Describe the morphology of the red blood cells.
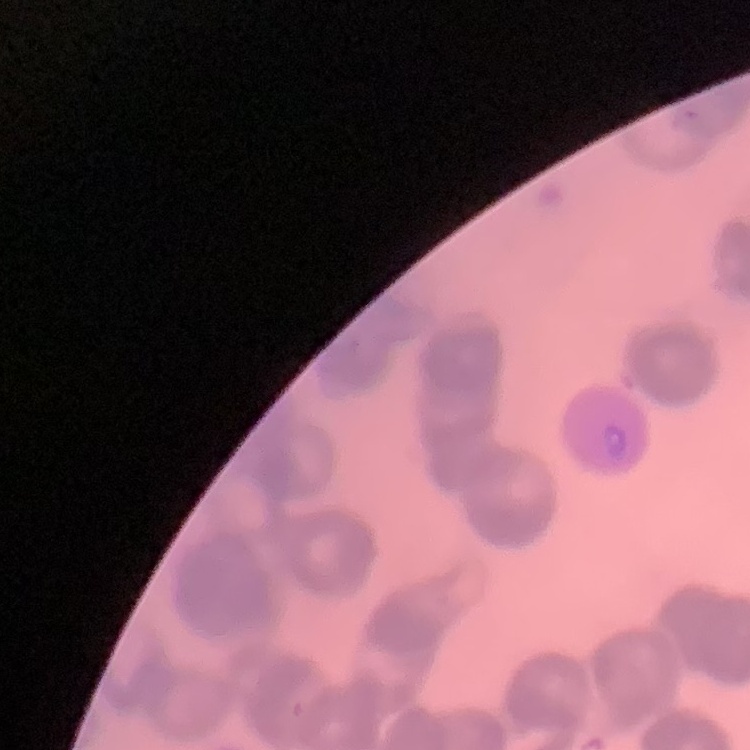

Rouleaux formation.

Summary:
  - Stain: Field's or Giemsa
  - Image type: square crop of a larger photomicrograph
  - Preparation: thin blood film